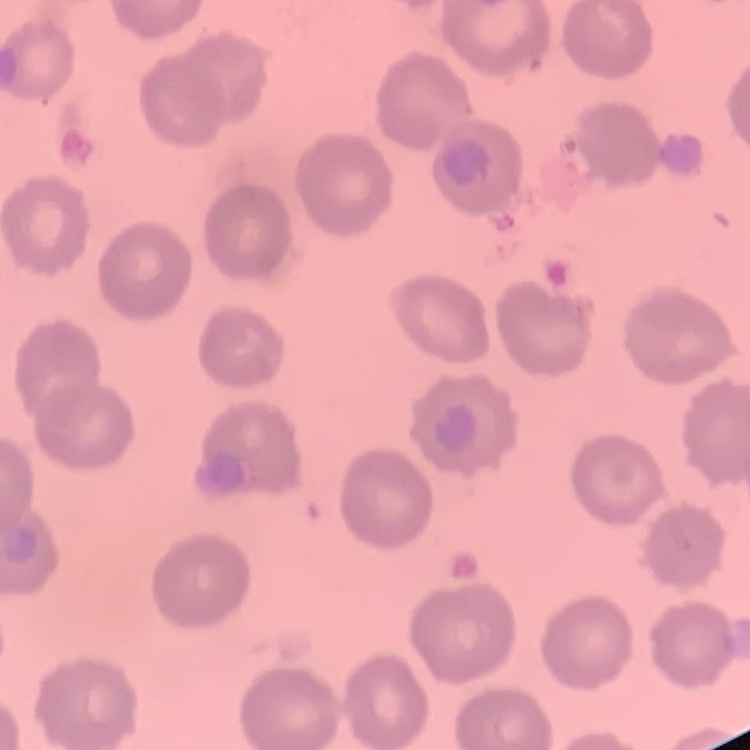

The red blood cells show no rouleaux formation. One tile cut from a larger photomicrograph. Stained with either Field's or Giemsa. Thin blood smear.